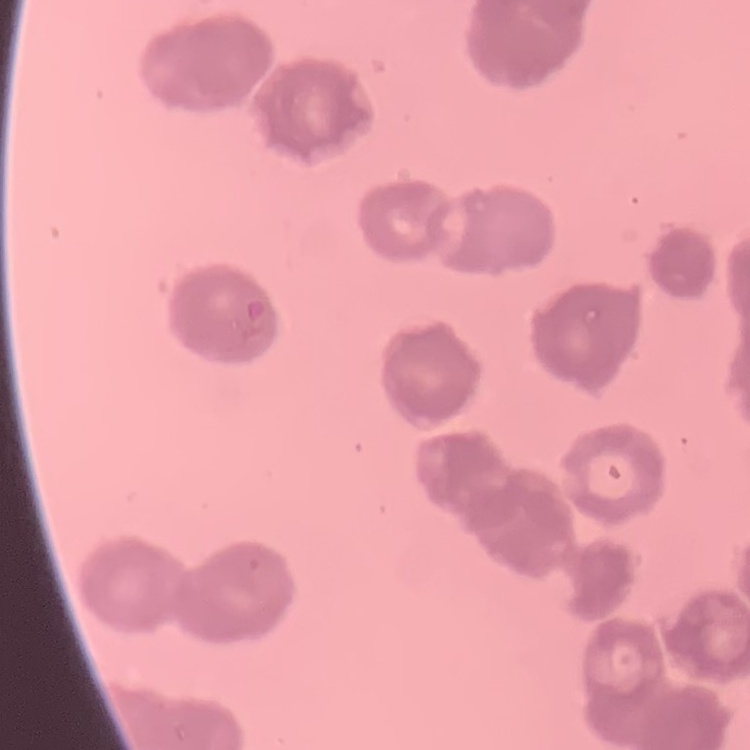

erythrocyte morphology = rouleaux formation
image type = square crop of a larger photomicrograph
preparation = thin blood smear
stain = Field's or Giemsa